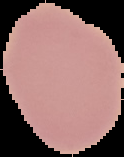
image size = 124×157 pixels
preparation = thin blood smear
image type = segmented cell region with the area outside set to black
result = no Plasmodium parasites detected